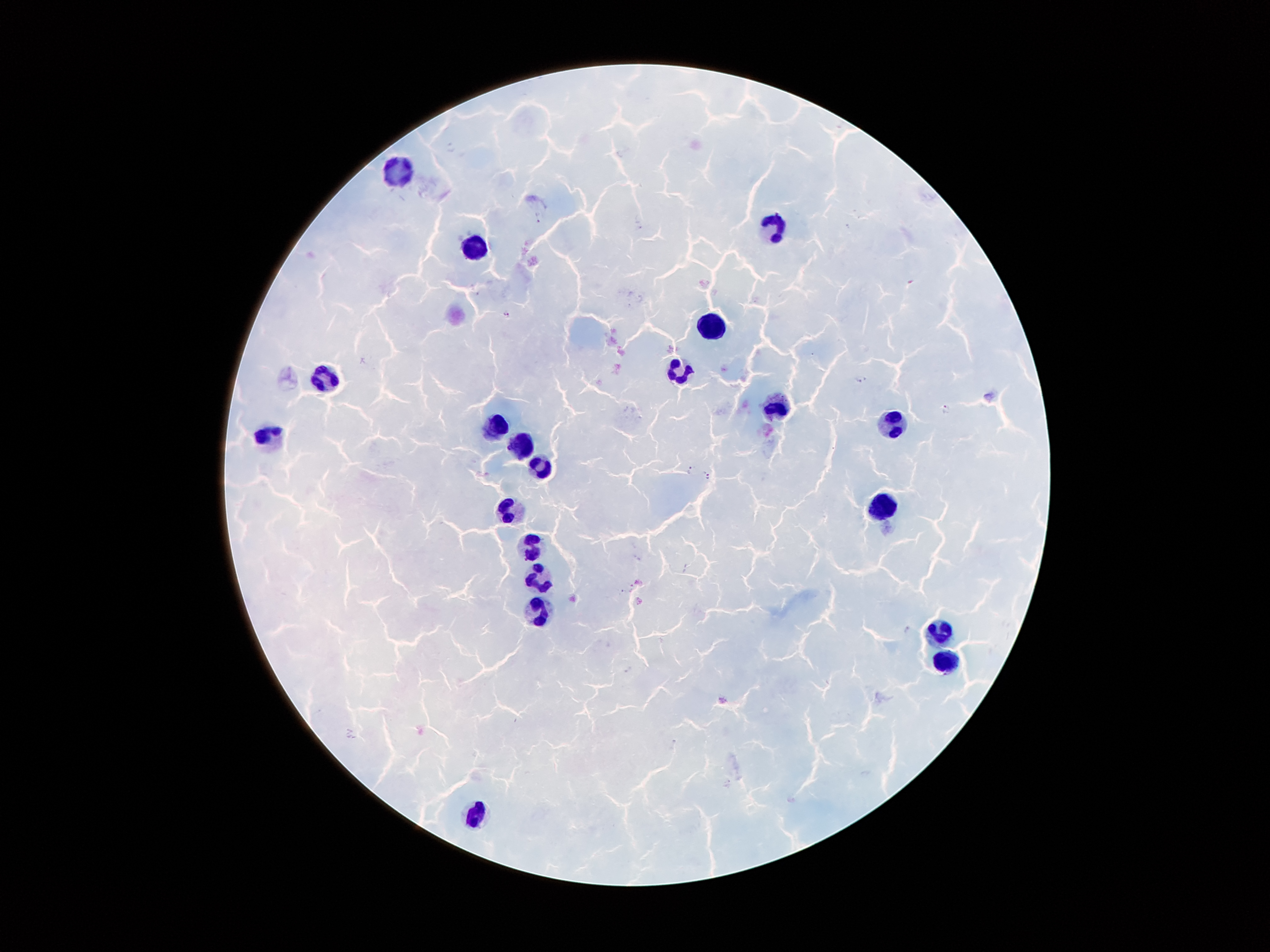
Approximate centers as (x, y) in pixels. Plasmodium parasite locations: (451, 146), (539, 217), (507, 313), (862, 380), (947, 408), (690, 470), (709, 475), (622, 591), (908, 630), (628, 669). Leukocyte locations: (402, 174), (774, 231), (473, 247), (708, 325), (678, 374), (325, 377), (774, 409), (892, 421), (501, 426), (267, 435), (521, 445), (544, 469), (508, 508), (882, 509), (529, 546), (539, 575), (540, 610), (937, 634), (944, 659), (474, 813). Thick blood smear. Giemsa stain. 100x magnification. One field from this slide. Photographed through the microscope eyepiece with a smartphone camera. Image is 1270×952 pixels. Patient malaria status: infected with Plasmodium falciparum.